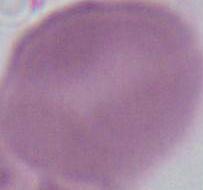

Summary:
  - Modality: photomicrograph
  - Identification: red blood cell
  - Magnification: 1000x